Name the blood parasite species.
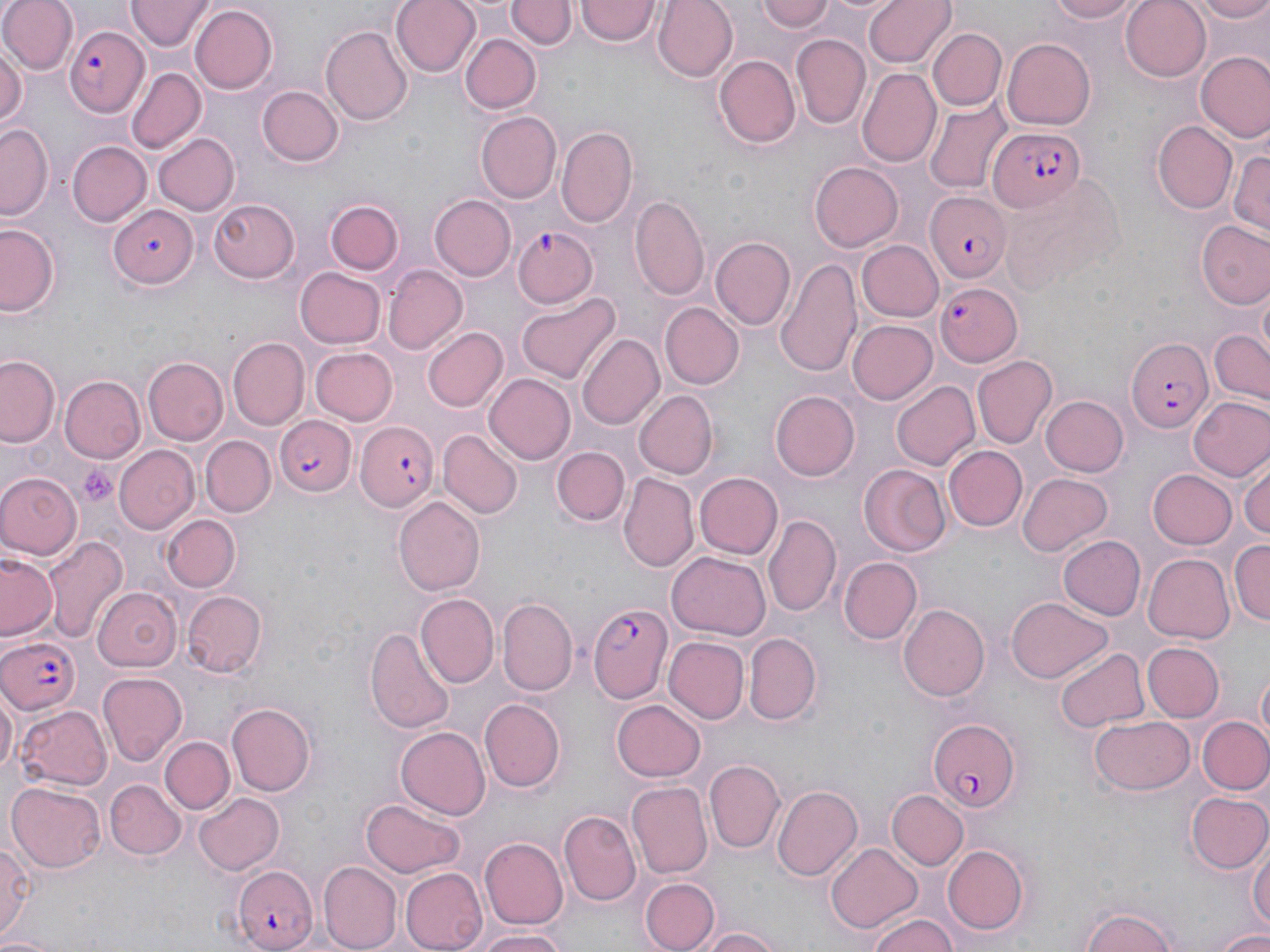
Plasmodium falciparum.

Approximate bounding boxes as [x1, y1, x2, y2] in pixels. Uninfected red blood cell locations: [1, 0, 76, 74], [127, 0, 212, 51], [391, 0, 482, 76], [652, 0, 736, 80], [756, 0, 837, 35], [864, 0, 954, 69], [1043, 0, 1139, 23], [1120, 0, 1211, 80], [1191, 0, 1270, 23], [507, 1, 572, 51], [575, 2, 659, 47], [1191, 4, 1269, 46], [189, 5, 276, 93], [322, 24, 413, 123], [928, 29, 1005, 110], [461, 32, 540, 114], [791, 34, 870, 129], [1003, 35, 1098, 129], [0, 42, 24, 135], [1195, 50, 1269, 143], [713, 54, 800, 149], [125, 66, 204, 152], [857, 68, 939, 169], [258, 86, 345, 168], [924, 104, 1011, 193], [476, 112, 561, 202], [1153, 121, 1238, 214], [1, 123, 51, 219], [556, 125, 640, 229], [153, 132, 239, 216], [66, 140, 150, 227], [1229, 142, 1269, 241], [810, 162, 903, 251], [428, 194, 515, 282], [631, 194, 709, 300], [324, 195, 406, 279], [207, 198, 301, 284], [1195, 220, 1270, 307], [0, 223, 62, 317], [710, 236, 796, 332], [855, 241, 942, 321], [776, 258, 862, 376], [296, 266, 386, 347], [382, 266, 465, 356], [516, 292, 620, 385], [661, 304, 743, 388], [848, 320, 938, 405], [423, 328, 508, 412], [1208, 328, 1270, 403], [579, 332, 665, 429], [228, 339, 308, 427], [311, 347, 398, 425], [971, 353, 1057, 449], [1, 355, 62, 448], [144, 357, 228, 445], [484, 374, 576, 464], [59, 375, 146, 463], [891, 382, 980, 470], [772, 389, 860, 479], [633, 390, 716, 479], [1040, 394, 1129, 477], [1189, 396, 1270, 483], [440, 430, 522, 518], [202, 436, 275, 517], [114, 444, 199, 532], [945, 445, 1026, 531], [554, 447, 627, 524], [1240, 452, 1270, 545], [859, 464, 952, 557], [1149, 470, 1237, 549], [693, 471, 783, 559], [620, 472, 699, 571], [0, 473, 82, 557], [1018, 473, 1112, 556], [393, 495, 485, 596], [162, 513, 239, 590], [764, 514, 840, 619], [43, 535, 126, 644], [1058, 535, 1145, 620], [1229, 538, 1269, 628], [668, 551, 770, 640], [1143, 553, 1234, 644], [0, 554, 58, 641], [839, 555, 922, 644], [91, 588, 180, 671], [182, 590, 268, 677], [415, 593, 498, 689], [1008, 596, 1110, 682], [497, 597, 577, 694], [899, 602, 990, 701], [367, 625, 456, 735], [745, 632, 822, 725], [663, 636, 749, 724], [1141, 642, 1223, 722], [1054, 645, 1146, 732], [97, 672, 188, 765], [1255, 672, 1270, 746], [0, 687, 18, 778], [479, 699, 565, 792], [611, 700, 706, 782], [228, 703, 314, 797], [16, 704, 113, 790], [1088, 715, 1195, 796], [1197, 715, 1270, 797], [395, 727, 491, 818], [161, 735, 235, 813], [705, 759, 783, 853], [7, 779, 106, 873], [106, 780, 185, 860], [629, 781, 711, 877], [772, 784, 863, 882], [887, 789, 969, 870], [193, 793, 285, 876], [1186, 793, 1270, 873], [360, 798, 469, 879], [559, 809, 641, 904], [1, 835, 34, 944], [480, 837, 569, 929], [1250, 837, 1269, 936], [825, 842, 925, 930], [941, 843, 1032, 936], [319, 861, 399, 951], [401, 865, 490, 952], [639, 877, 718, 952], [1079, 905, 1183, 952], [865, 911, 961, 952], [695, 926, 787, 952], [474, 928, 568, 952], [1216, 931, 1270, 952], [0, 933, 62, 952]. Platelet locations: [78, 465, 118, 506]. Plasmodium falciparum-infected red blood cell locations: [65, 26, 150, 114], [989, 127, 1085, 213], [922, 190, 1009, 285], [108, 205, 196, 288], [512, 223, 605, 306], [933, 282, 1021, 367], [1125, 339, 1211, 434], [275, 415, 355, 497], [356, 420, 437, 510], [590, 602, 672, 705], [0, 636, 82, 716], [928, 718, 1020, 814], [232, 864, 319, 952]. Image is 1270×952 pixels. Thin blood film. 1000x magnification. May-Grünwald-Giemsa-stained preparation. Light microscopy. One field of a larger specimen.